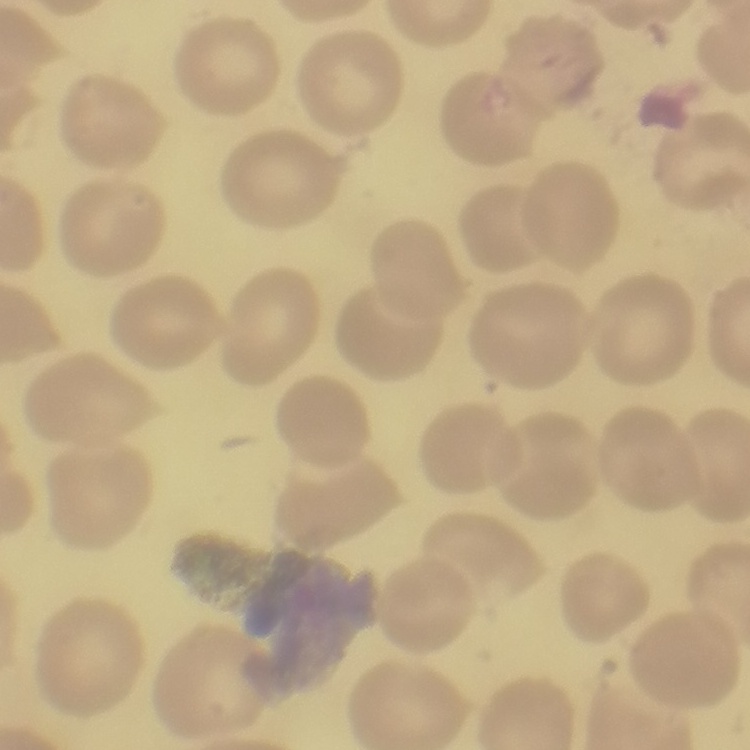

Summary:
  - Erythrocyte morphology: no rouleaux formation
  - Image type: square crop of a larger photomicrograph
  - Preparation: thin peripheral smear
  - Stain: Field's or Giemsa